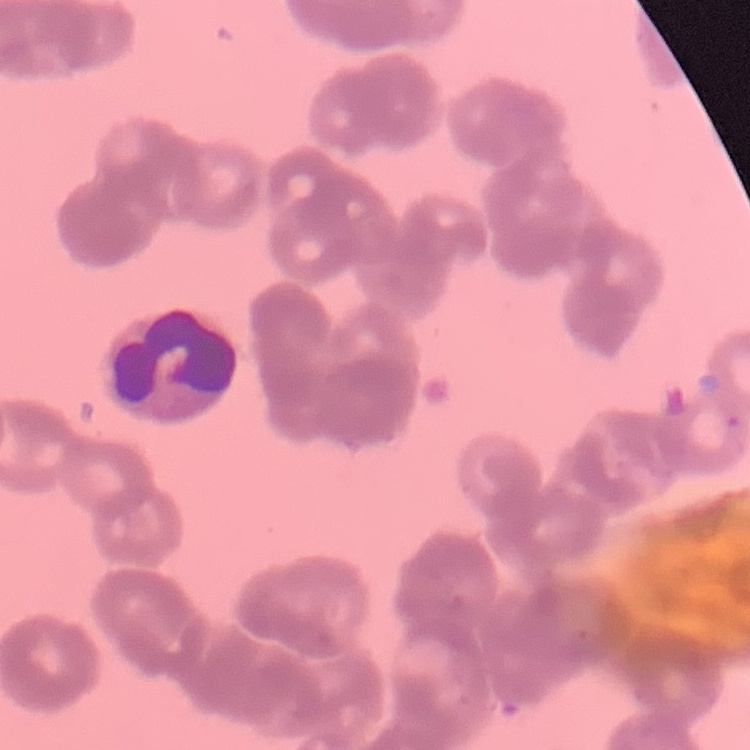
Summary:
  - Erythrocyte morphology: rouleaux formation
  - Preparation: thin peripheral smear
  - Stain: Field's or Giemsa
  - Image type: square crop of a larger photomicrograph